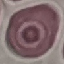
result = no malaria parasites detected
image type = automatically extracted cell patch, resized to 64 × 64 pixels
preparation = thin blood smear
stain = Giemsa
capture = smartphone camera at the microscope eyepiece